Classify this cell by malaria status.
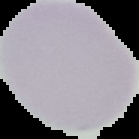
It is uninfected.

From a thin blood film. Cell region segmented out of the field of view; the surrounding area is masked to black. Image is 139×139 pixels.